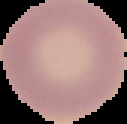 Malaria status: uninfected. The area outside the segmented cell region is set to black. From a thin blood smear. Image is 127×124 pixels.